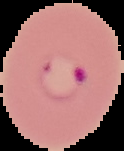

Summary:
  - Malaria status: parasitized
  - Preparation: thin blood film
  - Image type: segmented cell region with the area outside set to black
  - Image size: 124×151 pixels